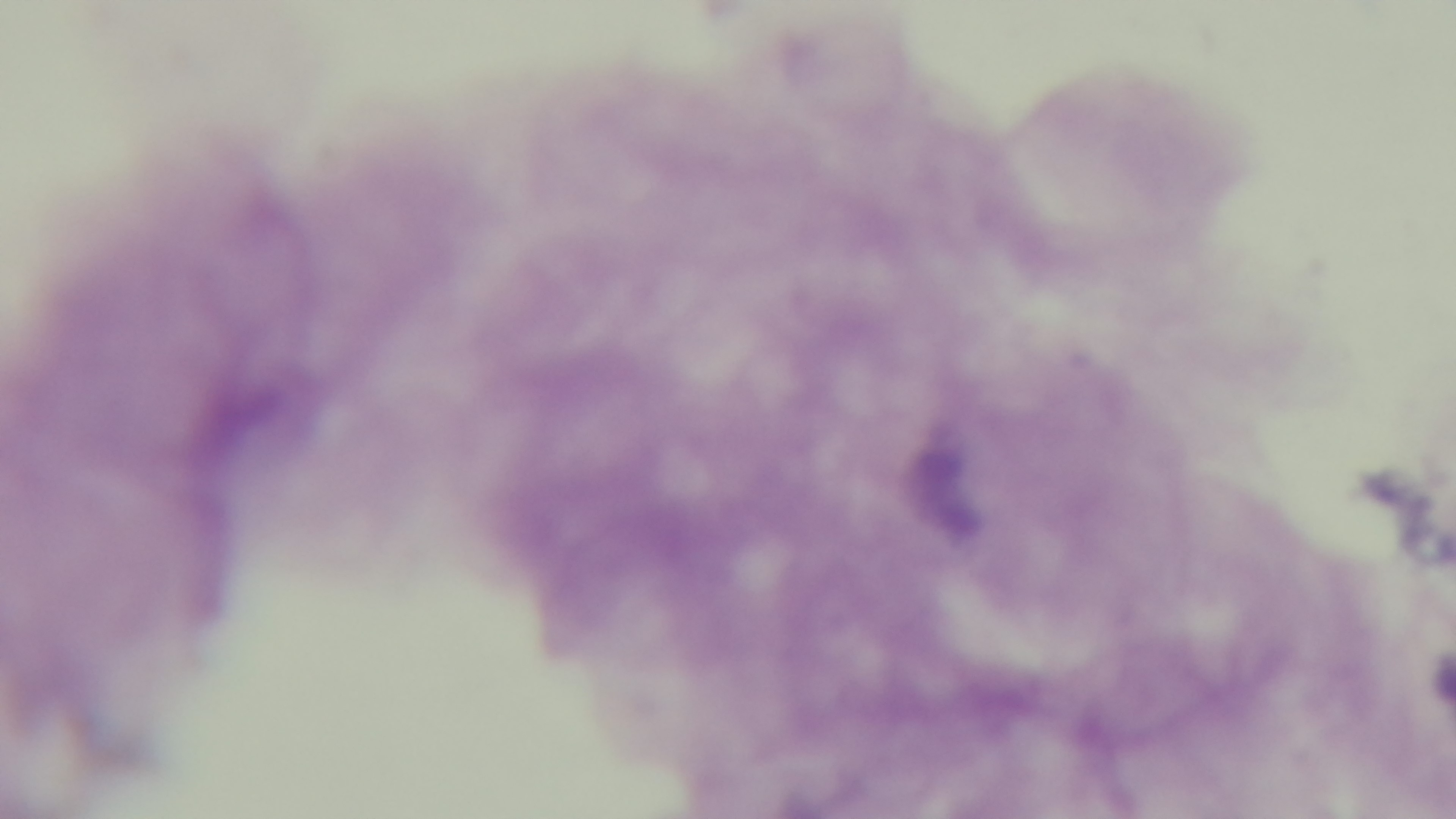
stain = Giemsa
preparation = thick blood film
capture = mounted 4K digital camera
objective = 100x oil immersion
modality = light microscopy
field of view = one from the slide
malaria status = uninfected